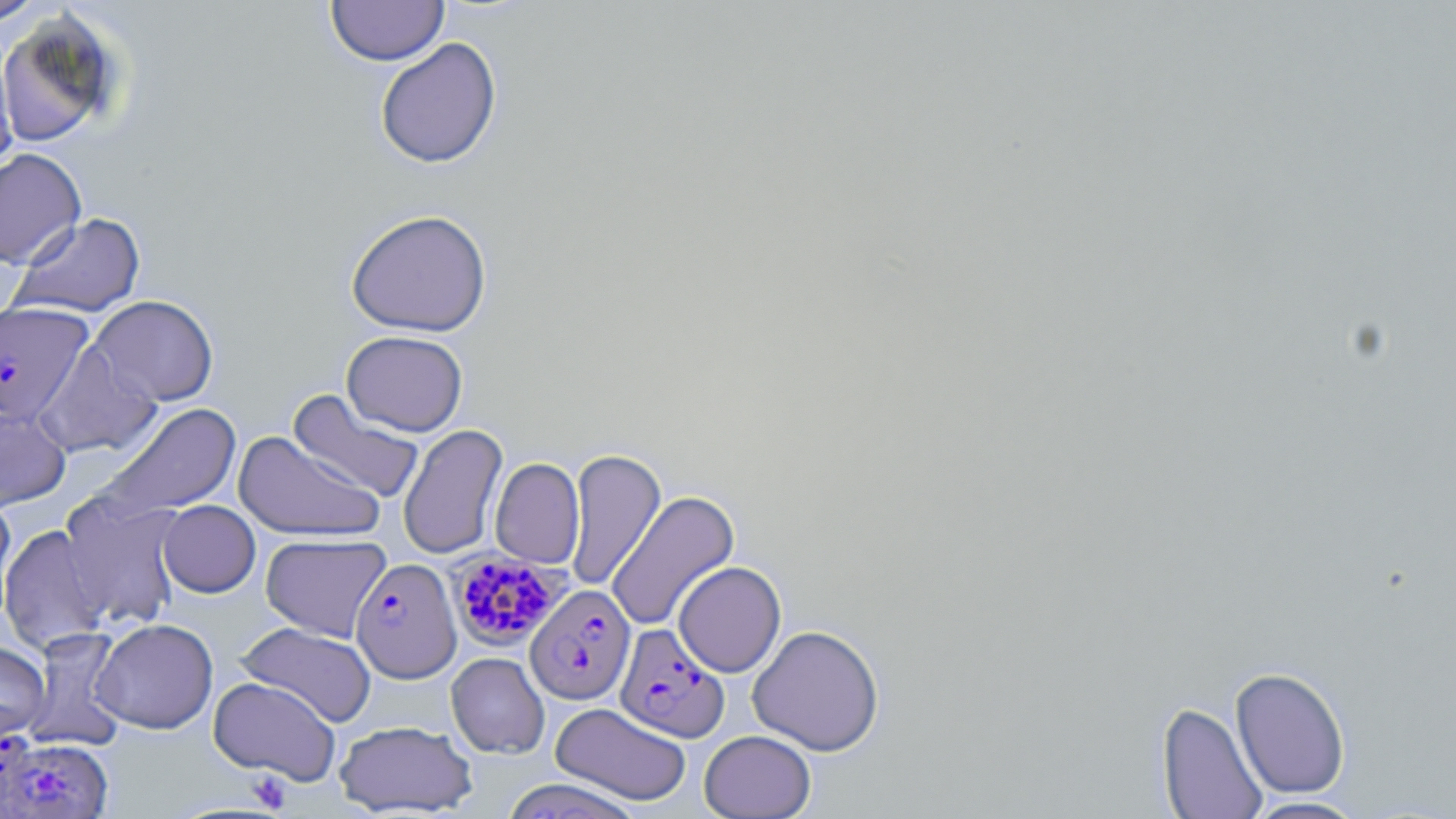

slide-level diagnosis = Plasmodium falciparum
modality = optical microscopy
Plasmodium falciparum-infected red blood cell locations = approximate bounding boxes as named x1/y1/x2/y2 corners in pixels: (x1=0, y1=301, x2=94, y2=426), (x1=448, y1=552, x2=566, y2=651), (x1=351, y1=558, x2=461, y2=684), (x1=525, y1=583, x2=636, y2=705), (x1=614, y1=623, x2=729, y2=742), (x1=0, y1=736, x2=111, y2=819)
field of view = single
uninfected red blood cell locations = approximate bounding boxes as named x1/y1/x2/y2 corners in pixels: (x1=326, y1=0, x2=448, y2=66), (x1=0, y1=1, x2=48, y2=25), (x1=0, y1=12, x2=125, y2=147), (x1=0, y1=37, x2=19, y2=179), (x1=375, y1=37, x2=502, y2=169), (x1=0, y1=148, x2=87, y2=268), (x1=345, y1=207, x2=493, y2=337), (x1=9, y1=212, x2=146, y2=318), (x1=87, y1=295, x2=219, y2=407), (x1=341, y1=330, x2=469, y2=436), (x1=33, y1=342, x2=163, y2=459), (x1=287, y1=389, x2=425, y2=504), (x1=99, y1=402, x2=242, y2=521), (x1=0, y1=404, x2=71, y2=511), (x1=397, y1=423, x2=508, y2=561), (x1=233, y1=431, x2=385, y2=542), (x1=564, y1=447, x2=666, y2=593), (x1=490, y1=457, x2=585, y2=569), (x1=606, y1=489, x2=740, y2=632), (x1=59, y1=490, x2=187, y2=630), (x1=0, y1=493, x2=17, y2=628), (x1=157, y1=500, x2=260, y2=598), (x1=0, y1=524, x2=111, y2=654), (x1=260, y1=533, x2=391, y2=642), (x1=673, y1=561, x2=787, y2=678), (x1=91, y1=618, x2=218, y2=734), (x1=235, y1=622, x2=377, y2=727), (x1=747, y1=623, x2=885, y2=756), (x1=24, y1=627, x2=130, y2=751), (x1=0, y1=641, x2=50, y2=745), (x1=446, y1=652, x2=549, y2=759), (x1=1230, y1=666, x2=1351, y2=799), (x1=207, y1=676, x2=341, y2=784), (x1=1156, y1=701, x2=1268, y2=818), (x1=551, y1=702, x2=692, y2=806), (x1=334, y1=720, x2=478, y2=816), (x1=699, y1=730, x2=816, y2=818), (x1=498, y1=778, x2=649, y2=818), (x1=1241, y1=796, x2=1370, y2=818)
platelet locations = approximate bounding boxes as named x1/y1/x2/y2 corners in pixels: (x1=246, y1=771, x2=293, y2=813)
stain = May-Grünwald-Giemsa
magnification = 1000x
preparation = thin blood film
image size = 1456×819 pixels